Assess the morphology of the red blood cells.
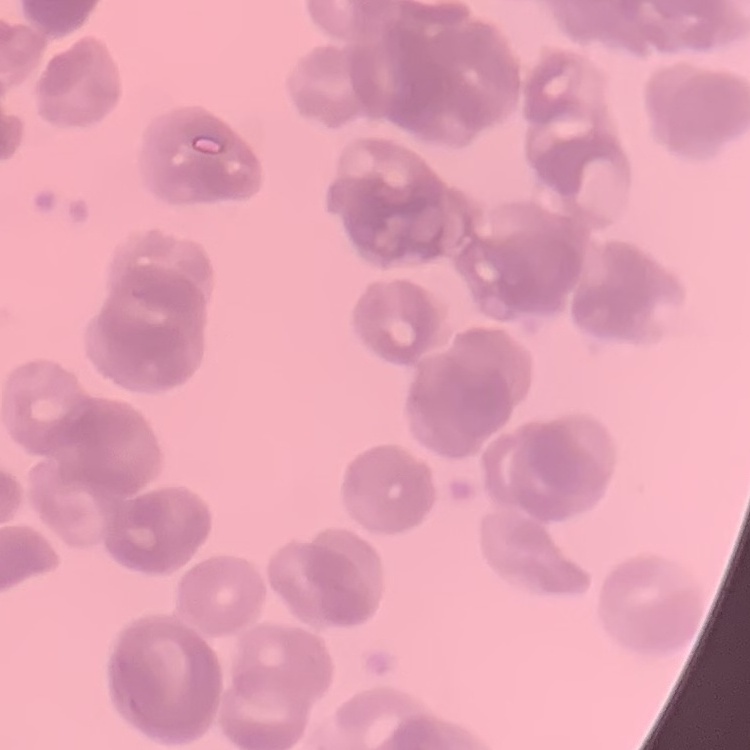
Rouleaux formation.

Summary:
  - Image type: square crop of a larger photomicrograph
  - Preparation: thin peripheral smear
  - Stain: Field's or Giemsa